Locate and identify every blood parasite.
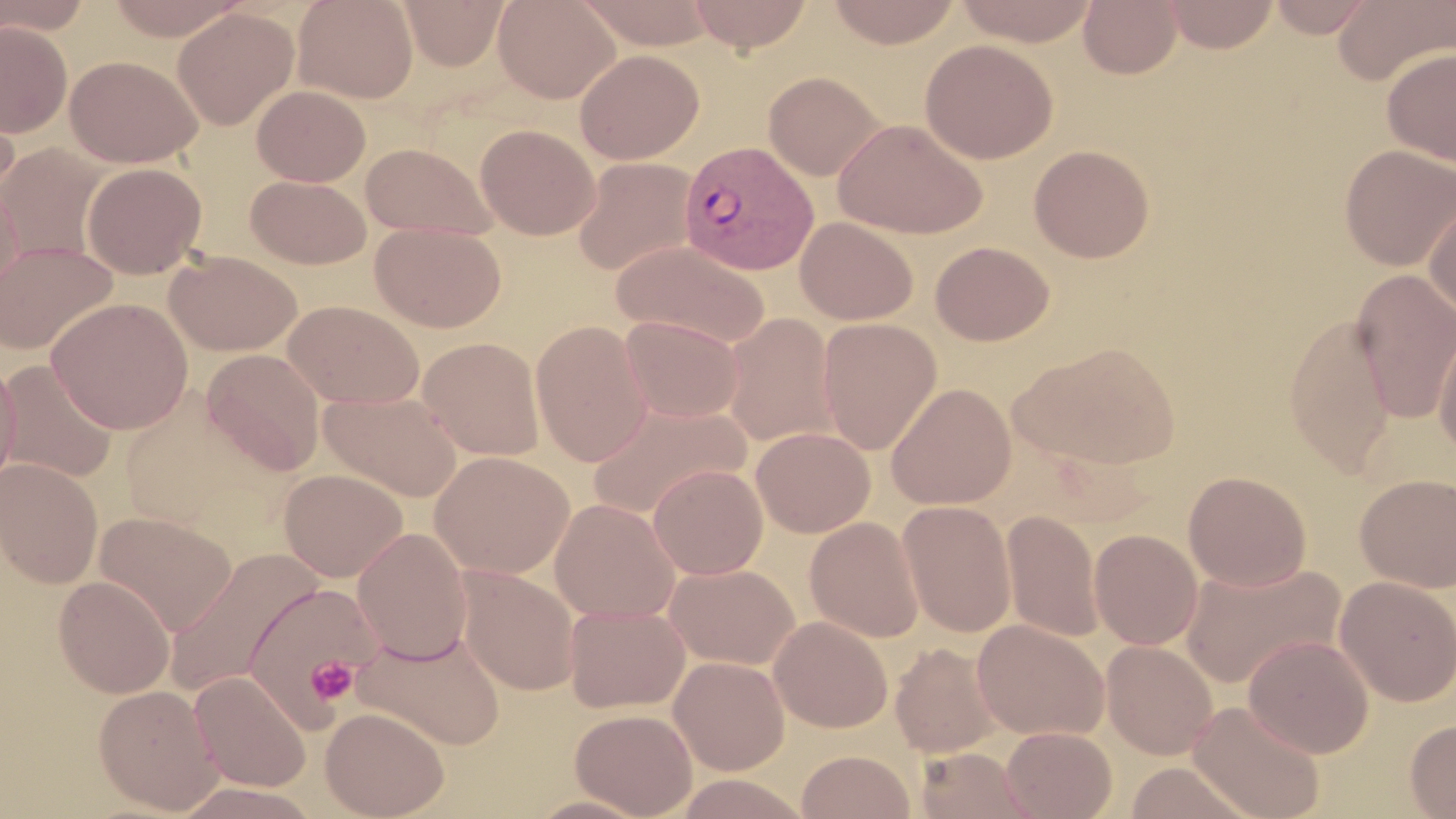
Approximate bounding boxes as [x1, y1, x2, y2] in pixels.
Plasmodium vivax-infected red blood cells: [678, 141, 819, 276].
No Plasmodium falciparum, Plasmodium ovale, Plasmodium malariae, Babesia divergens, or Trypanosoma brucei observed.

Uninfected red blood cell locations: [0, 0, 91, 37], [103, 0, 251, 40], [292, 0, 419, 103], [399, 0, 510, 71], [493, 0, 620, 103], [575, 0, 719, 49], [687, 0, 814, 52], [825, 0, 963, 48], [952, 0, 1101, 46], [1078, 0, 1183, 79], [1160, 0, 1280, 53], [1266, 0, 1379, 38], [1333, 0, 1456, 86], [172, 7, 298, 130], [0, 21, 73, 138], [920, 39, 1058, 164], [1382, 47, 1456, 168], [574, 49, 704, 164], [65, 54, 203, 168], [763, 71, 886, 181], [0, 80, 20, 206], [251, 85, 370, 186], [833, 118, 988, 239], [475, 123, 600, 240], [360, 142, 499, 241], [0, 143, 109, 265], [1028, 144, 1155, 263], [1338, 144, 1456, 271], [572, 157, 698, 278], [81, 162, 207, 279], [245, 175, 371, 268], [0, 178, 24, 298], [1423, 191, 1456, 323], [795, 217, 919, 325], [369, 221, 507, 333], [0, 240, 117, 355], [612, 240, 771, 349], [930, 241, 1054, 346], [164, 249, 302, 356], [1350, 268, 1456, 425], [47, 297, 194, 434], [283, 300, 424, 409], [722, 312, 839, 450], [1284, 312, 1396, 477], [620, 315, 743, 423], [817, 318, 942, 454], [1433, 318, 1456, 461], [530, 319, 653, 467], [418, 336, 545, 461], [1011, 342, 1183, 470], [202, 349, 327, 476], [0, 358, 21, 489], [0, 360, 117, 483], [886, 383, 1016, 509], [320, 390, 462, 502], [585, 399, 752, 520], [751, 426, 875, 537], [431, 451, 574, 578], [0, 457, 104, 588], [648, 464, 768, 580], [279, 468, 408, 582], [1183, 471, 1311, 591], [1354, 473, 1456, 593], [549, 498, 681, 622], [897, 501, 1017, 637], [94, 510, 236, 635], [1003, 510, 1104, 643], [804, 517, 925, 642], [352, 527, 473, 664], [1089, 529, 1203, 650], [164, 549, 322, 699], [1179, 559, 1346, 691], [663, 562, 799, 669], [458, 566, 581, 696], [53, 575, 175, 698], [1334, 576, 1456, 706], [243, 581, 380, 727], [564, 603, 691, 714], [769, 615, 893, 733], [972, 619, 1109, 740], [352, 625, 506, 751], [1243, 634, 1374, 758], [1101, 639, 1218, 759], [889, 642, 1006, 758], [669, 656, 791, 775], [189, 671, 311, 792], [93, 684, 223, 813], [1187, 699, 1327, 819], [319, 706, 450, 819], [569, 708, 698, 818], [1404, 717, 1456, 818], [1001, 726, 1117, 819], [914, 746, 1037, 819], [796, 750, 916, 818], [1121, 761, 1258, 819]. Platelet locations: [305, 656, 358, 705]. Slide-level diagnosis: Plasmodium vivax. 1000x magnification. Thin blood film. May-Grünwald-Giemsa stain. Image is 1456×819 pixels. One field of a larger specimen. Light microscopy.